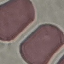
Result: no malaria parasites detected. Cell patch, automatically extracted from a larger field of view and resized to 64 × 64 pixels. Thin blood film. Giemsa stain. Photographed with a smartphone camera at the microscope eyepiece.